Assess this cell for malaria.
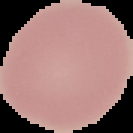
It is uninfected.

image size = 133×133 pixels
preparation = thin blood film
image type = segmented cell region with the area outside set to black